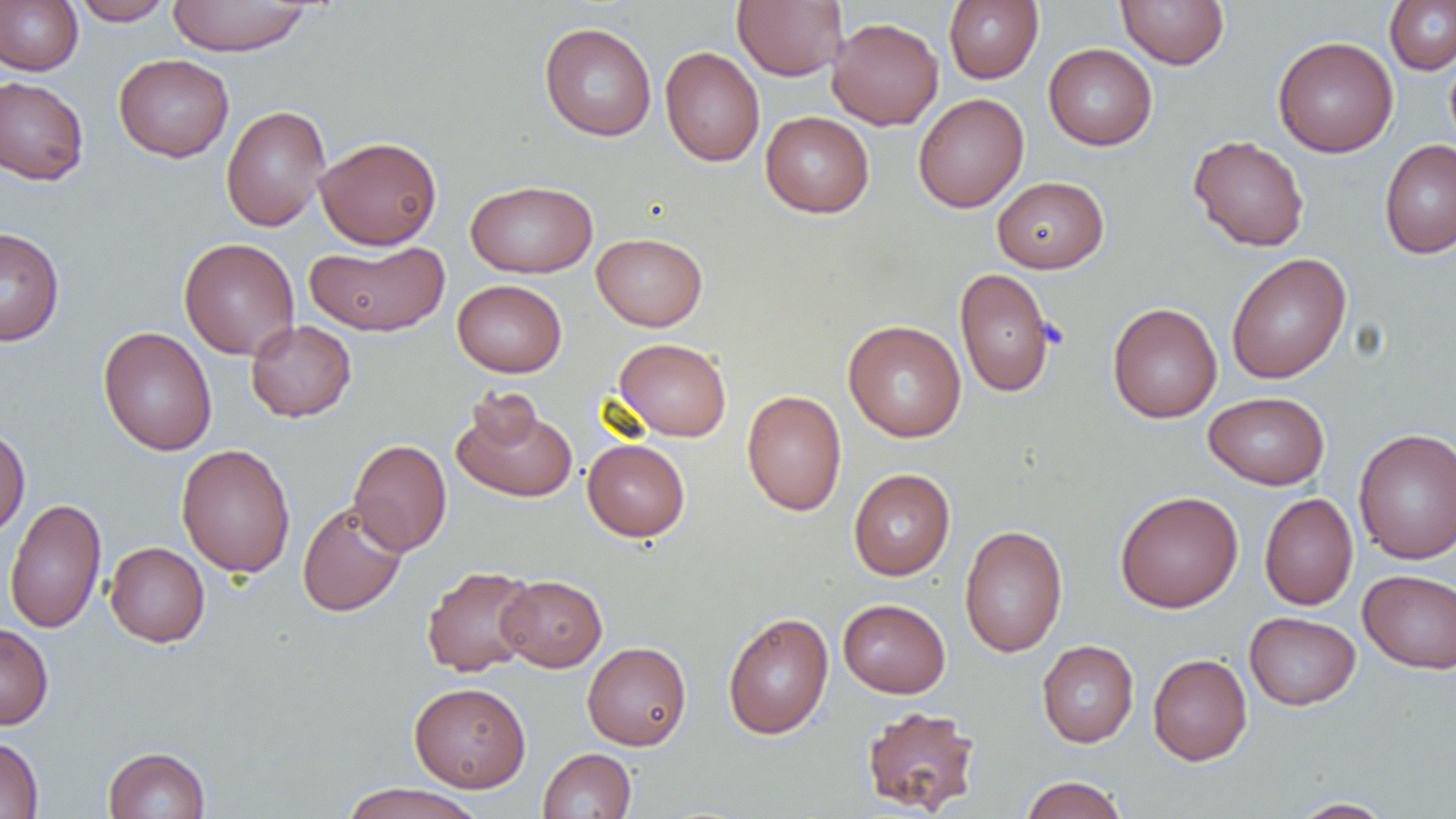

slide-level diagnosis = negative for blood parasites
magnification = 1000x
uninfected red blood cell locations = approximate bounding boxes as (x1,y1)-(x2,y2) corner pairs in pixels: (0,0)-(83,75), (71,0)-(175,26), (166,0)-(312,56), (944,0)-(1043,84), (1116,0)-(1229,69), (732,1)-(847,81), (1384,1)-(1456,74), (827,17)-(944,130), (539,22)-(657,141), (1272,36)-(1399,157), (1044,43)-(1157,150), (660,46)-(765,167), (113,53)-(234,162), (0,76)-(89,185), (913,93)-(1029,213), (221,104)-(331,231), (760,111)-(874,218), (314,135)-(442,249), (1188,135)-(1310,251), (1379,139)-(1456,258), (992,176)-(1109,274), (465,179)-(598,278), (0,227)-(65,346), (591,233)-(708,331), (178,237)-(300,360), (305,239)-(449,337), (1226,253)-(1352,384), (954,267)-(1056,397), (452,280)-(566,377), (1107,302)-(1222,423), (246,320)-(356,422), (843,320)-(967,442), (98,326)-(217,456), (614,337)-(732,441), (742,390)-(847,516), (1203,391)-(1330,490), (451,395)-(578,503), (0,424)-(30,540), (1353,427)-(1456,564), (348,439)-(452,556), (582,439)-(690,541), (176,444)-(295,578), (848,468)-(955,580), (1115,490)-(1243,613), (1259,493)-(1358,610), (5,498)-(106,634), (297,500)-(408,617), (959,524)-(1068,657), (105,542)-(210,647), (421,565)-(538,677), (1358,569)-(1456,673), (497,575)-(607,671), (838,598)-(951,698), (1244,611)-(1361,710), (722,612)-(834,739), (0,623)-(53,729), (1037,640)-(1138,747), (582,641)-(691,750), (1148,653)-(1252,765), (409,681)-(531,792), (861,705)-(981,815), (0,735)-(43,818), (103,746)-(210,819), (538,747)-(636,819), (1019,776)-(1128,819), (339,783)-(486,819), (1289,798)-(1395,818)
modality = light microscopy
field of view = single
preparation = thin blood film
image size = 1456×819 pixels